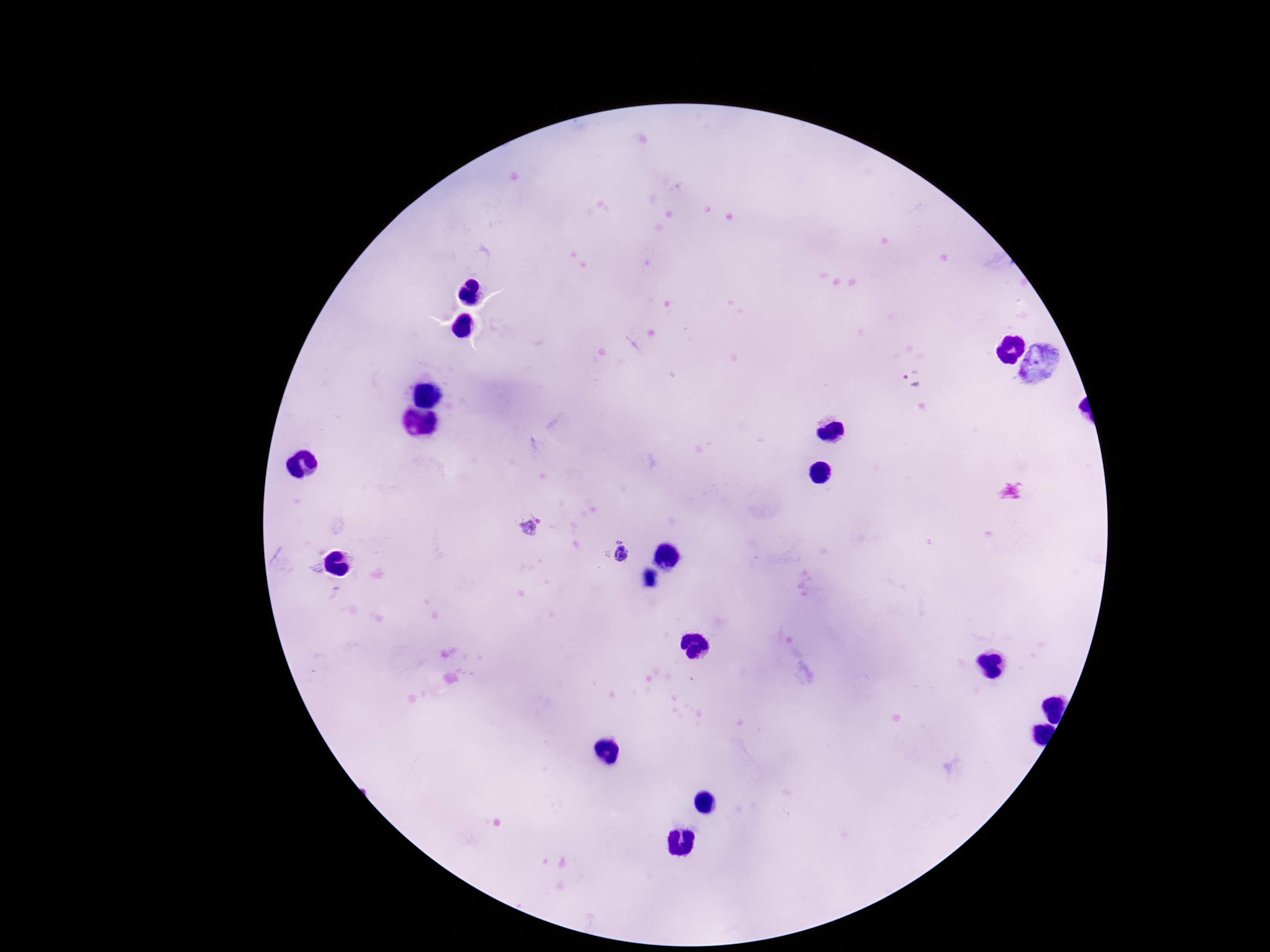

Approximate centers as (x, y) in pixels. Plasmodium parasite locations: (912, 380), (538, 519), (528, 529), (617, 539), (622, 553). Giemsa-stained preparation. 100x magnification. Thick blood film. Patient malaria status: infected. Image is 1270×952 pixels. One field from this slide. Photographed through the microscope eyepiece with a smartphone camera.